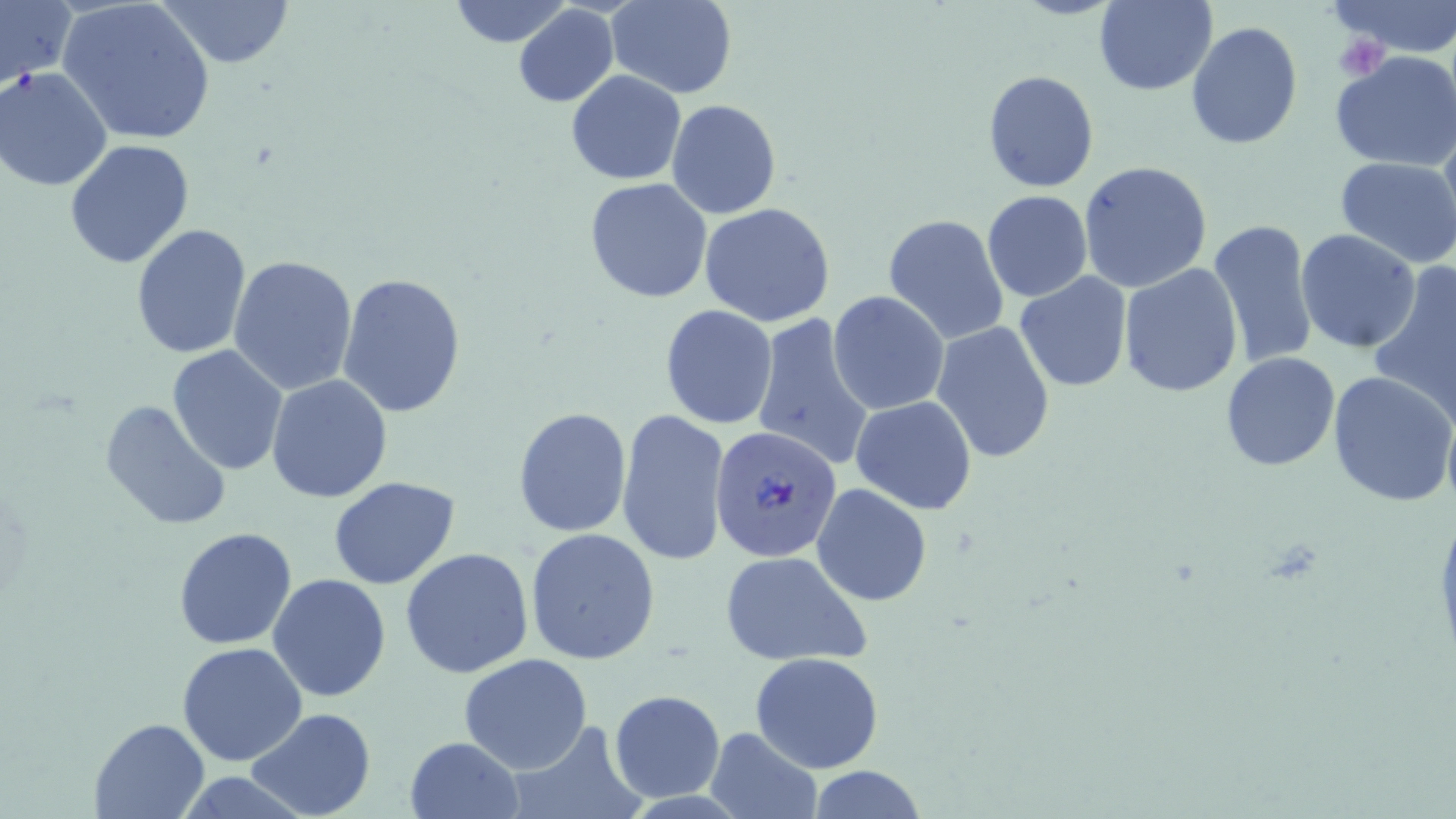

Summary:
  - Coordinate format: approximate bounding boxes as (x1, y1, x2, y2) in pixels
  - Uninfected red blood cell locations: (0, 0, 76, 86), (58, 0, 217, 146), (156, 0, 294, 70), (446, 0, 573, 47), (607, 0, 737, 98), (1329, 0, 1456, 56), (1094, 1, 1218, 95), (513, 4, 619, 108), (1186, 22, 1303, 151), (1331, 50, 1456, 171), (1, 66, 116, 192), (567, 69, 686, 184), (981, 69, 1101, 194), (666, 100, 782, 220), (1439, 109, 1456, 248), (66, 137, 197, 268), (1334, 156, 1456, 267), (1077, 161, 1213, 292), (584, 178, 713, 302), (982, 190, 1093, 303), (698, 201, 836, 327), (882, 213, 1010, 344), (1208, 219, 1318, 368), (130, 222, 252, 359), (1295, 228, 1422, 353), (229, 256, 360, 397), (1118, 263, 1244, 397), (1366, 268, 1456, 426), (337, 271, 468, 419), (1014, 273, 1133, 392), (828, 291, 950, 415), (659, 306, 778, 428), (751, 313, 874, 471), (931, 321, 1056, 464), (167, 344, 290, 477), (1220, 351, 1341, 471), (1328, 371, 1454, 505), (266, 374, 394, 504), (850, 396, 978, 515), (100, 399, 234, 531), (512, 407, 633, 538), (616, 409, 730, 567), (328, 476, 460, 589), (811, 483, 931, 607), (172, 526, 298, 649), (524, 528, 662, 666), (400, 549, 534, 680), (719, 550, 872, 668), (267, 573, 392, 703), (176, 641, 308, 767), (751, 651, 883, 774), (460, 654, 593, 773), (608, 688, 725, 803), (247, 708, 375, 819), (89, 716, 210, 819), (503, 721, 644, 819), (705, 729, 821, 818), (405, 736, 522, 818), (805, 766, 927, 819)
  - Plasmodium falciparum-infected red blood cell locations: (712, 425, 840, 560)
  - Platelet locations: (1332, 34, 1390, 82)
  - Slide-level diagnosis: Plasmodium falciparum
  - Image size: 1456×819 pixels
  - Stain: May-Grünwald-Giemsa
  - Modality: optical microscopy
  - Preparation: thin blood film
  - Field of view: single
  - Magnification: 1000x